Locate every Plasmodium parasite and every leukocyte.
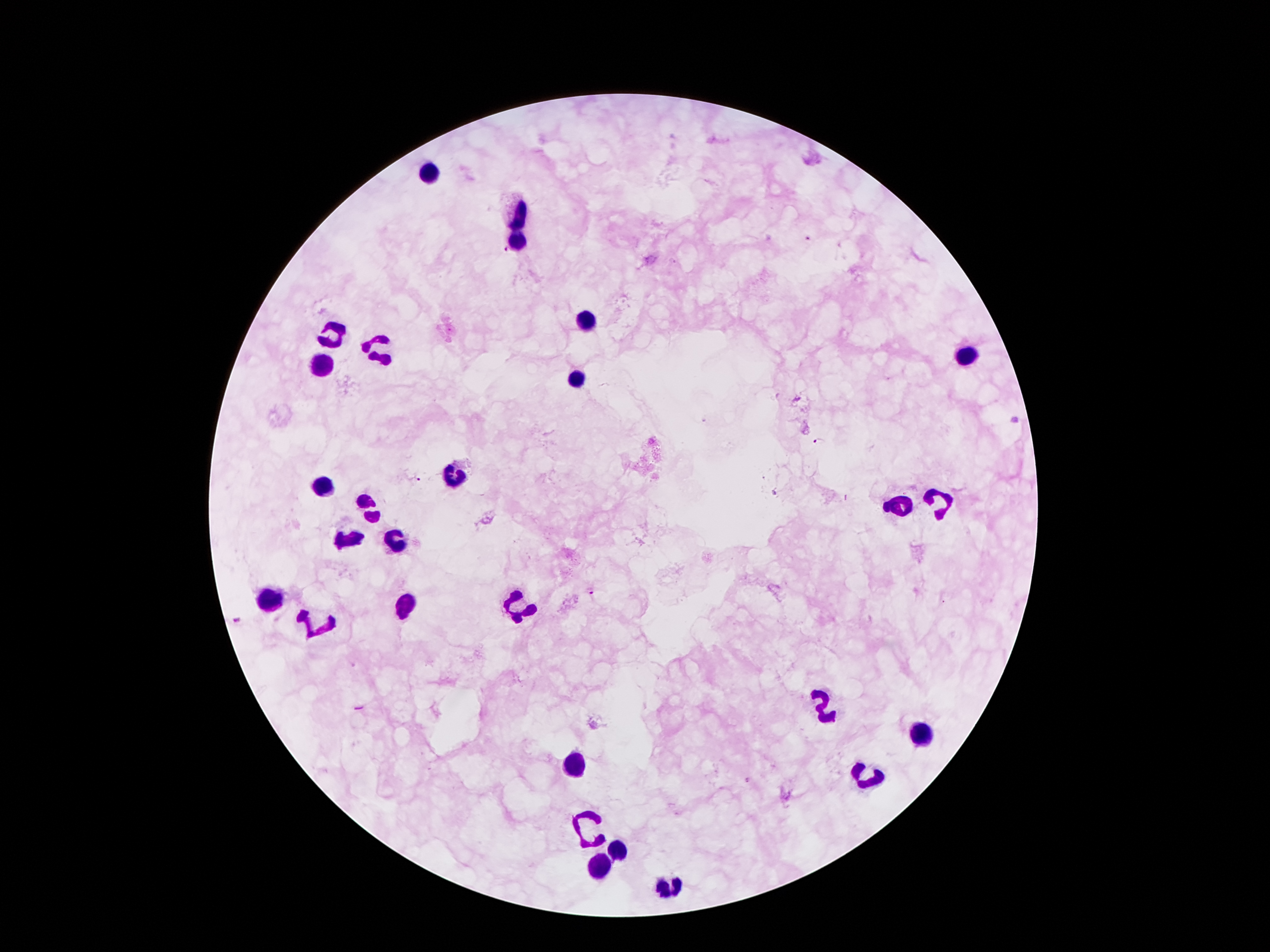
Approximate object centers, in pixels from the top-left corner.
Plasmodium parasites: (x=809, y=239), (x=503, y=253), (x=817, y=442), (x=415, y=480), (x=590, y=591), (x=237, y=619).
Leukocytes: (x=430, y=174), (x=520, y=213), (x=517, y=242), (x=587, y=320), (x=328, y=333), (x=380, y=350), (x=965, y=356), (x=320, y=363), (x=577, y=380), (x=455, y=474), (x=323, y=486), (x=938, y=501), (x=901, y=504), (x=370, y=507), (x=350, y=539), (x=397, y=540), (x=269, y=599), (x=404, y=605), (x=517, y=605), (x=316, y=626), (x=826, y=705), (x=919, y=737), (x=575, y=764), (x=863, y=782), (x=589, y=825), (x=617, y=851), (x=599, y=867), (x=668, y=888).

Photographed through the microscope eyepiece with a smartphone camera. Image is 1270×952 pixels. Patient malaria status: positive for Plasmodium falciparum. Single field of view. Thick blood smear. 100x magnification. Giemsa-stained preparation.